Outline each blood parasite and name the species.
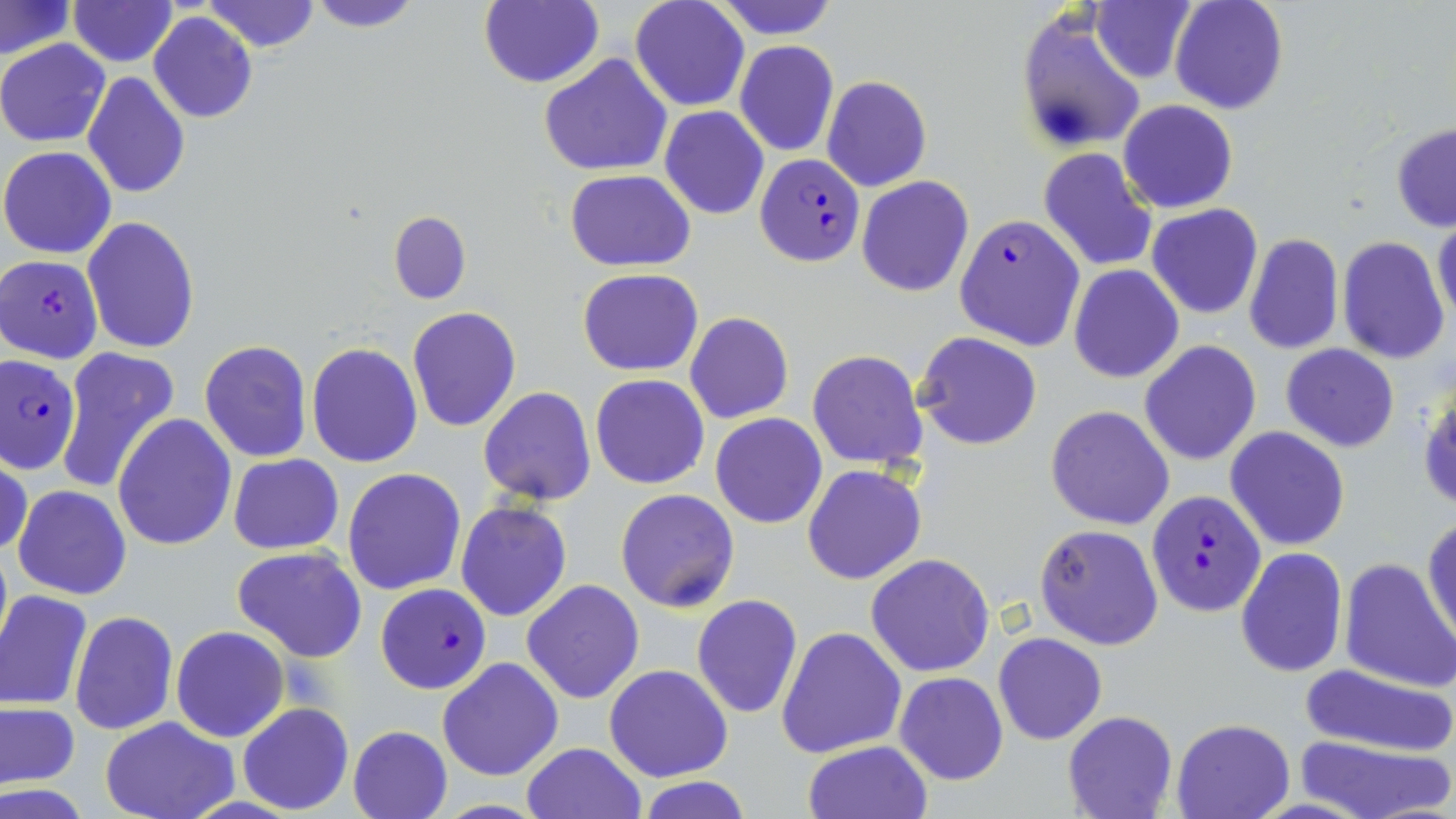

Approximate bounding boxes as (x1, y1, x2, y2) in pixels.
Plasmodium falciparum-infected red blood cells: (754, 155, 864, 266), (954, 214, 1084, 351), (1, 255, 103, 364), (0, 357, 81, 474), (1147, 490, 1267, 617), (375, 583, 488, 694).
No Plasmodium ovale, Plasmodium malariae, Plasmodium vivax, Babesia divergens, or Trypanosoma brucei observed.

Summary:
  - Uninfected red blood cell locations: (201, 0, 321, 53), (306, 0, 424, 31), (478, 0, 603, 89), (629, 0, 749, 110), (712, 0, 840, 39), (1091, 0, 1197, 84), (1169, 0, 1289, 114), (68, 1, 176, 66), (1, 2, 74, 59), (1016, 9, 1148, 156), (149, 11, 257, 123), (0, 39, 110, 148), (734, 40, 839, 158), (540, 54, 673, 177), (82, 72, 190, 197), (822, 75, 932, 192), (1119, 99, 1237, 213), (661, 107, 768, 219), (1390, 123, 1456, 232), (1, 146, 116, 258), (1039, 147, 1157, 271), (25, 162, 154, 307), (565, 169, 695, 272), (857, 176, 972, 296), (1147, 203, 1264, 319), (388, 212, 470, 304), (1433, 212, 1456, 329), (82, 217, 200, 354), (1243, 234, 1344, 355), (1337, 236, 1450, 363), (1069, 265, 1183, 383), (577, 268, 703, 377), (408, 307, 521, 432), (685, 312, 794, 423), (915, 332, 1041, 450), (199, 339, 313, 464), (1139, 339, 1261, 466), (1282, 342, 1399, 453), (306, 343, 423, 467), (55, 347, 182, 496), (808, 350, 928, 469), (590, 375, 711, 490), (1418, 379, 1456, 517), (479, 387, 596, 507), (1046, 405, 1175, 531), (711, 413, 826, 528), (113, 414, 237, 550), (1226, 426, 1350, 550), (1, 454, 31, 561), (228, 454, 343, 554), (804, 464, 927, 585), (343, 467, 467, 596), (13, 484, 131, 601), (615, 489, 740, 612), (456, 500, 573, 622), (1424, 515, 1456, 650), (1036, 524, 1163, 650), (233, 546, 368, 662), (1235, 547, 1348, 678), (866, 553, 996, 677), (1338, 557, 1455, 693), (521, 579, 645, 704), (0, 591, 94, 711), (692, 594, 804, 719), (409, 608, 532, 753), (69, 610, 178, 736), (777, 625, 906, 760), (170, 626, 288, 742), (994, 632, 1107, 745), (437, 657, 565, 779), (604, 664, 733, 782), (1296, 664, 1456, 758), (894, 672, 1009, 786), (1, 702, 79, 789), (238, 703, 354, 815), (1062, 710, 1178, 819), (99, 715, 240, 819), (1171, 718, 1294, 819), (347, 726, 452, 819), (1295, 735, 1453, 819), (802, 740, 932, 818), (520, 742, 648, 819), (632, 777, 755, 818)
  - Slide-level diagnosis: Plasmodium falciparum
  - Field of view: single
  - Image size: 1456×819 pixels
  - Magnification: 1000x
  - Modality: optical microscopy
  - Preparation: thin blood smear
  - Stain: May-Grünwald-Giemsa